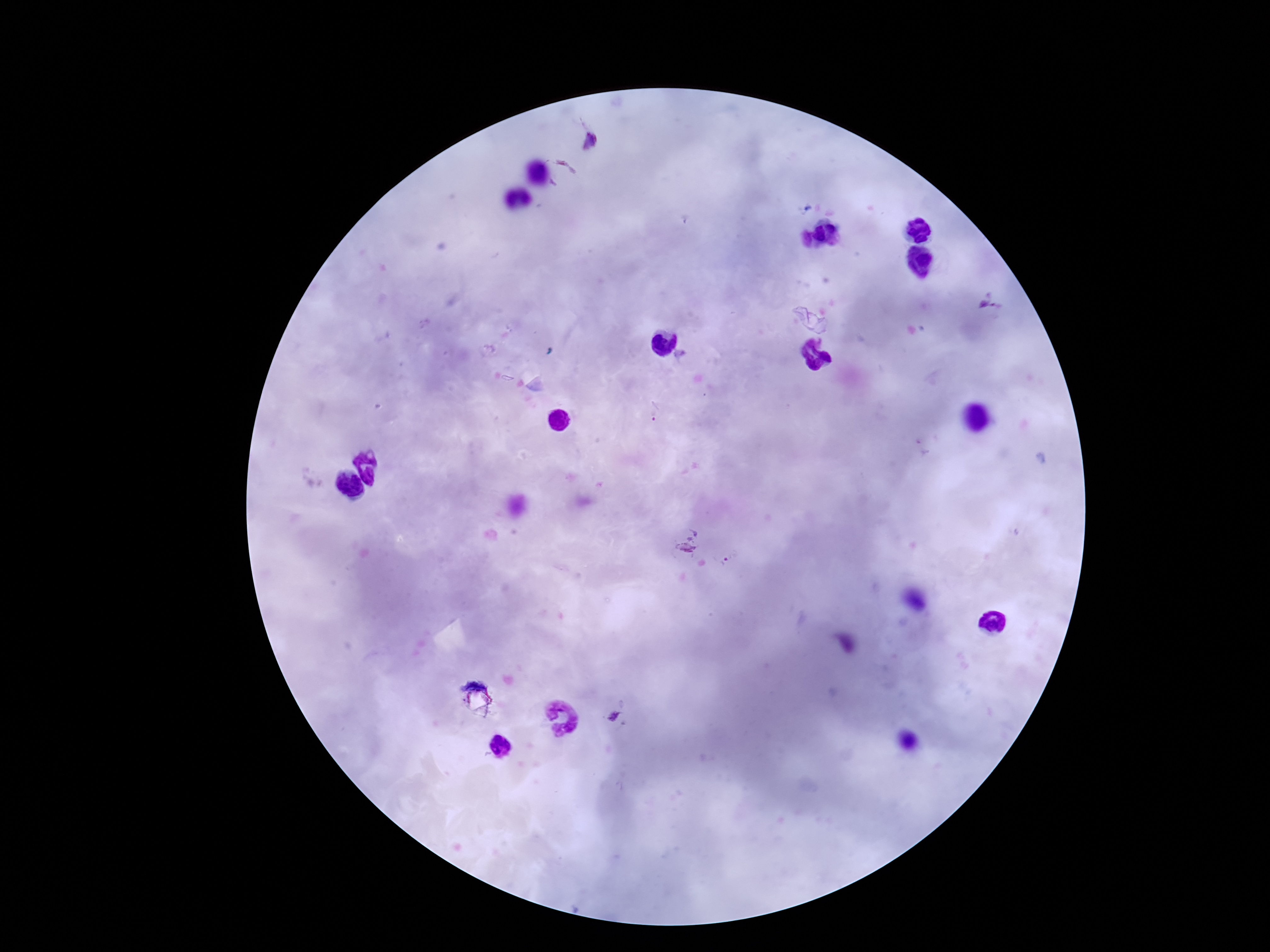 Approximate object centers, in pixels from the top-left corner. Plasmodium parasite locations: (x=590, y=141), (x=560, y=173), (x=989, y=303), (x=653, y=412), (x=684, y=539), (x=724, y=561), (x=614, y=717). 100x magnification. Thick blood smear. One field from this slide. Image is 1270×952 pixels. Patient malaria status: infected. Photographed through the microscope eyepiece with a smartphone camera. Giemsa-stained preparation.